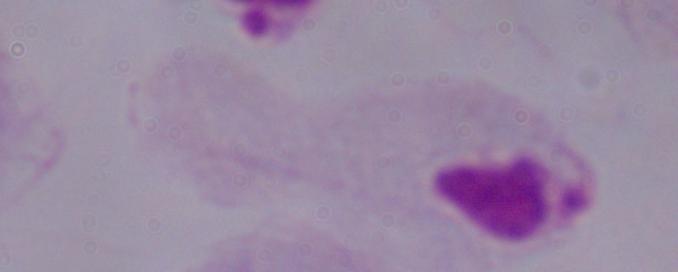 A trichomonad is shown. Micrograph. 1000x magnification.